Point out cells.
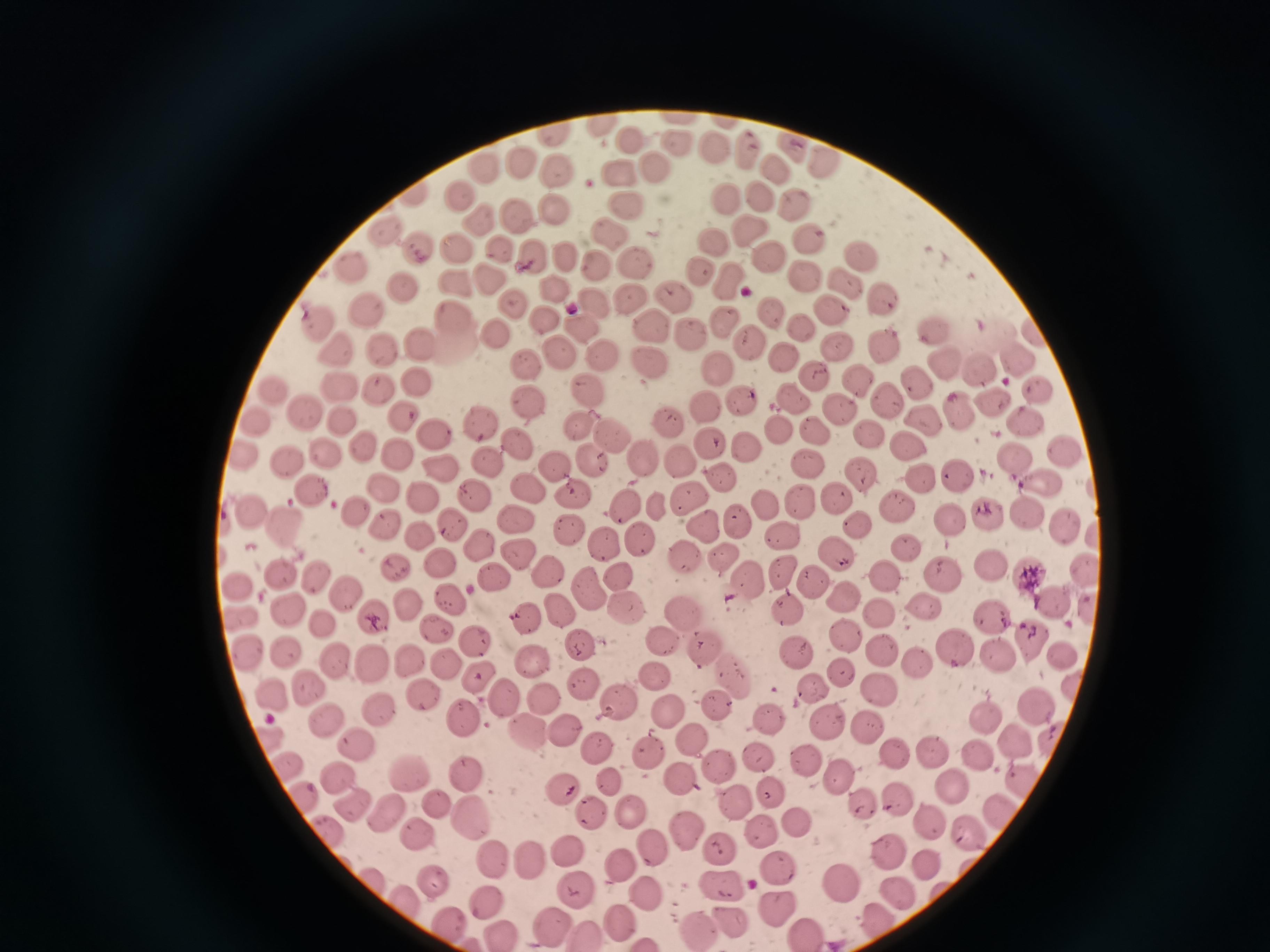
Approximate object centers, in pixels from the top-left corner.
Cells: (x=604, y=124), (x=634, y=140), (x=789, y=144), (x=679, y=146), (x=747, y=147), (x=717, y=148), (x=824, y=159), (x=522, y=165), (x=772, y=166), (x=488, y=168), (x=558, y=168), (x=655, y=170), (x=617, y=171), (x=761, y=193), (x=460, y=195), (x=728, y=196), (x=798, y=202), (x=556, y=207), (x=626, y=207), (x=511, y=213), (x=478, y=219), (x=747, y=229), (x=386, y=232), (x=606, y=232), (x=807, y=238), (x=710, y=244), (x=420, y=247), (x=499, y=248), (x=455, y=251), (x=533, y=253), (x=767, y=256), (x=858, y=257), (x=564, y=258), (x=597, y=259), (x=637, y=260), (x=350, y=265), (x=699, y=272), (x=727, y=276), (x=809, y=277), (x=489, y=282), (x=847, y=283), (x=401, y=285), (x=558, y=290), (x=634, y=291), (x=882, y=296), (x=673, y=297), (x=513, y=301), (x=592, y=302), (x=829, y=308), (x=370, y=309), (x=775, y=311), (x=451, y=317), (x=543, y=317), (x=317, y=318), (x=722, y=321), (x=655, y=323), (x=581, y=325), (x=934, y=326), (x=496, y=329), (x=802, y=331), (x=689, y=333), (x=751, y=339), (x=419, y=341), (x=839, y=344), (x=882, y=345), (x=380, y=347), (x=336, y=351), (x=781, y=353), (x=560, y=354), (x=601, y=354), (x=1020, y=360), (x=649, y=362), (x=946, y=364), (x=529, y=366), (x=980, y=366), (x=718, y=367), (x=814, y=374), (x=855, y=374), (x=917, y=380), (x=422, y=381), (x=341, y=384), (x=381, y=390), (x=587, y=390), (x=276, y=392), (x=1038, y=394), (x=792, y=395), (x=527, y=397), (x=887, y=397), (x=741, y=402), (x=995, y=403), (x=706, y=406), (x=839, y=407), (x=304, y=410), (x=961, y=410), (x=340, y=418), (x=401, y=418), (x=670, y=420), (x=481, y=421), (x=257, y=422), (x=925, y=423), (x=1027, y=424), (x=577, y=425), (x=777, y=425), (x=813, y=430), (x=437, y=434), (x=611, y=434), (x=867, y=436), (x=708, y=440), (x=519, y=441), (x=913, y=446), (x=360, y=447), (x=746, y=447), (x=329, y=452), (x=242, y=454), (x=1067, y=454), (x=399, y=455), (x=1014, y=455), (x=679, y=458), (x=806, y=458), (x=488, y=459), (x=642, y=459), (x=289, y=461), (x=592, y=461), (x=439, y=467), (x=560, y=468), (x=858, y=471), (x=717, y=475), (x=953, y=476), (x=919, y=478), (x=1041, y=483), (x=389, y=486), (x=529, y=487), (x=313, y=490), (x=475, y=492), (x=577, y=492), (x=686, y=496), (x=426, y=498), (x=832, y=498), (x=800, y=502), (x=622, y=503), (x=763, y=504), (x=656, y=505), (x=896, y=505), (x=253, y=507), (x=358, y=509), (x=1024, y=513), (x=988, y=515), (x=516, y=517), (x=735, y=519), (x=949, y=520), (x=281, y=522), (x=854, y=522), (x=389, y=524), (x=455, y=524), (x=703, y=524), (x=1066, y=526), (x=567, y=528), (x=783, y=536), (x=641, y=538), (x=599, y=541), (x=483, y=545), (x=904, y=546), (x=519, y=549), (x=836, y=551), (x=684, y=554), (x=721, y=559), (x=439, y=564), (x=993, y=566), (x=1087, y=566), (x=399, y=567), (x=285, y=569), (x=549, y=571), (x=780, y=573), (x=942, y=573), (x=883, y=574), (x=498, y=575), (x=1032, y=575), (x=315, y=576), (x=618, y=577), (x=746, y=579), (x=812, y=583), (x=238, y=587), (x=341, y=590), (x=588, y=590), (x=451, y=594), (x=843, y=598), (x=1053, y=601), (x=409, y=602), (x=922, y=605), (x=1091, y=607), (x=560, y=610), (x=625, y=610), (x=877, y=610), (x=293, y=612), (x=788, y=612), (x=684, y=613), (x=523, y=614), (x=377, y=615), (x=993, y=615), (x=241, y=619), (x=325, y=625), (x=436, y=630), (x=848, y=636), (x=477, y=640), (x=662, y=640), (x=1028, y=640), (x=582, y=641), (x=704, y=645), (x=953, y=645), (x=285, y=649), (x=880, y=649), (x=1066, y=651), (x=245, y=653), (x=335, y=653), (x=794, y=653), (x=994, y=653), (x=536, y=656), (x=409, y=658), (x=377, y=659), (x=918, y=660), (x=445, y=664), (x=842, y=667), (x=734, y=671), (x=655, y=672), (x=474, y=675), (x=306, y=683), (x=583, y=684), (x=811, y=685), (x=877, y=687), (x=420, y=689), (x=272, y=693), (x=505, y=695), (x=542, y=697), (x=617, y=701), (x=1033, y=703), (x=720, y=704), (x=380, y=708), (x=666, y=712), (x=985, y=712), (x=771, y=716), (x=467, y=717), (x=330, y=719), (x=826, y=720), (x=869, y=723), (x=560, y=728), (x=521, y=729), (x=271, y=737), (x=690, y=738), (x=1018, y=741), (x=359, y=742), (x=1051, y=743), (x=598, y=744), (x=645, y=745), (x=933, y=750), (x=894, y=753), (x=980, y=755), (x=763, y=758), (x=810, y=759), (x=717, y=762), (x=284, y=765), (x=335, y=774), (x=408, y=774), (x=467, y=774), (x=677, y=774), (x=606, y=777), (x=844, y=778), (x=950, y=783), (x=561, y=786), (x=1024, y=786), (x=775, y=792), (x=301, y=795), (x=898, y=798), (x=735, y=799), (x=354, y=804), (x=437, y=805), (x=864, y=805), (x=998, y=805), (x=627, y=809), (x=590, y=810), (x=385, y=811), (x=473, y=812), (x=929, y=821), (x=797, y=826), (x=327, y=828), (x=682, y=829), (x=968, y=831), (x=764, y=834), (x=416, y=837), (x=720, y=845), (x=652, y=846), (x=570, y=850), (x=889, y=852), (x=532, y=857), (x=492, y=858), (x=620, y=863), (x=928, y=866), (x=779, y=868), (x=371, y=878), (x=434, y=880), (x=842, y=882), (x=578, y=886), (x=723, y=888), (x=649, y=891), (x=898, y=891), (x=489, y=899), (x=775, y=902), (x=411, y=903), (x=620, y=918), (x=727, y=918), (x=873, y=919), (x=449, y=921), (x=553, y=921), (x=697, y=925), (x=584, y=927), (x=499, y=931), (x=807, y=932).

Acquired by smartphone through the microscope eyepiece. Giemsa-stained preparation. One field from this slide. Thin blood smear. Image is 1270×952 pixels.